Outline each blood parasite and name the species.
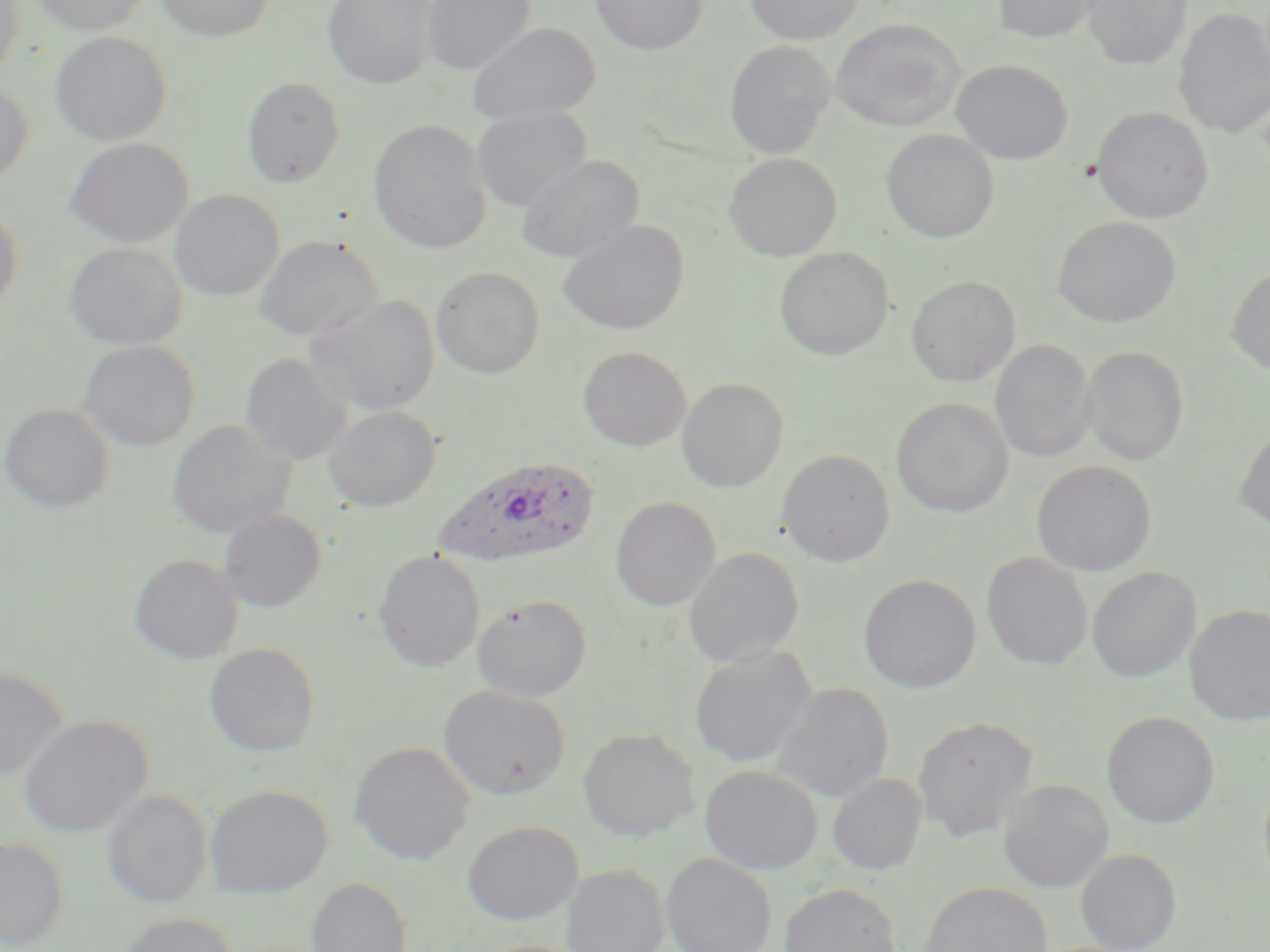

Approximate bounding boxes as (x1, y1, x2, y2) in pixels.
Plasmodium ovale-infected red blood cells: (432, 455, 600, 572).
No Plasmodium falciparum, Plasmodium malariae, Plasmodium vivax, Babesia divergens, or Trypanosoma brucei observed.

Uninfected red blood cell locations: (0, 0, 25, 82), (30, 0, 152, 35), (154, 0, 276, 42), (323, 0, 439, 90), (421, 0, 536, 76), (590, 0, 709, 56), (744, 0, 865, 44), (1082, 0, 1192, 70), (991, 1, 1101, 44), (1173, 8, 1270, 140), (831, 18, 966, 131), (467, 22, 601, 125), (50, 31, 172, 146), (724, 40, 835, 158), (951, 59, 1073, 164), (241, 76, 346, 187), (0, 80, 33, 186), (1091, 105, 1214, 224), (472, 106, 592, 212), (368, 119, 490, 253), (881, 129, 999, 243), (63, 137, 194, 248), (724, 153, 842, 261), (516, 154, 645, 263), (169, 190, 285, 302), (0, 207, 23, 315), (1053, 216, 1180, 328), (557, 219, 689, 336), (253, 234, 384, 341), (64, 242, 186, 351), (774, 247, 894, 360), (430, 265, 545, 378), (1226, 266, 1270, 375), (906, 275, 1021, 387), (305, 293, 440, 416), (991, 338, 1096, 463), (79, 341, 200, 451), (1082, 345, 1189, 466), (578, 346, 691, 452), (240, 353, 352, 465), (676, 377, 789, 493), (891, 397, 1014, 518), (1, 404, 114, 513), (324, 406, 441, 512), (166, 420, 294, 539), (1234, 423, 1270, 532), (777, 448, 896, 566), (1032, 461, 1157, 576), (610, 496, 720, 611), (217, 509, 327, 613), (683, 546, 805, 667), (372, 550, 487, 673), (981, 552, 1094, 671), (129, 554, 243, 664), (1086, 566, 1202, 682), (858, 574, 981, 694), (472, 594, 592, 703), (1185, 604, 1270, 725), (204, 642, 321, 757), (689, 646, 817, 767), (0, 666, 68, 785), (772, 682, 894, 803), (439, 685, 570, 800), (1101, 711, 1220, 829), (19, 715, 153, 838), (912, 715, 1039, 842), (577, 727, 700, 841), (349, 740, 475, 866), (699, 765, 823, 875), (1258, 769, 1270, 894), (827, 772, 927, 876), (998, 778, 1114, 893), (205, 784, 332, 898), (103, 790, 213, 909), (462, 820, 583, 925), (1, 838, 68, 950), (1075, 848, 1182, 952), (660, 852, 776, 952), (562, 863, 670, 952), (305, 877, 413, 952), (779, 881, 901, 952), (919, 881, 1051, 952), (116, 912, 239, 952), (472, 938, 592, 952). Slide-level diagnosis: Plasmodium ovale. Single field of view. Thin blood film. Optical microscopy. May-Grünwald-Giemsa stain. Image is 1270×952 pixels. Captured at 1000x magnification.